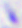 Toxoplasma gondii is seen. Photomicrograph. 400x magnification.